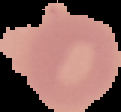 Cell region segmented out of the field of view; the surrounding area is masked to black. Malaria status: uninfected. Image is 121×112 pixels. From a thin blood smear.